Name the parasite shown.
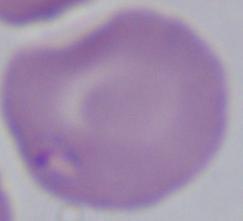

This is Babesia.

magnification = 1000x
modality = photomicrograph